Assess this cell for malaria.
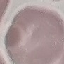

It is uninfected.

Summary:
  - Preparation: thin blood smear
  - Image type: automatically extracted cell patch, resized to 64 × 64 pixels
  - Capture: smartphone through the microscope eyepiece
  - Stain: Giemsa